Assess this cell for malaria.
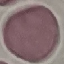
Uninfected.

Giemsa-stained preparation. Automatically extracted cell patch, resized to 64 × 64 pixels. Thin smear of blood. Acquired by smartphone through the microscope eyepiece.